Locate and identify every blood parasite.
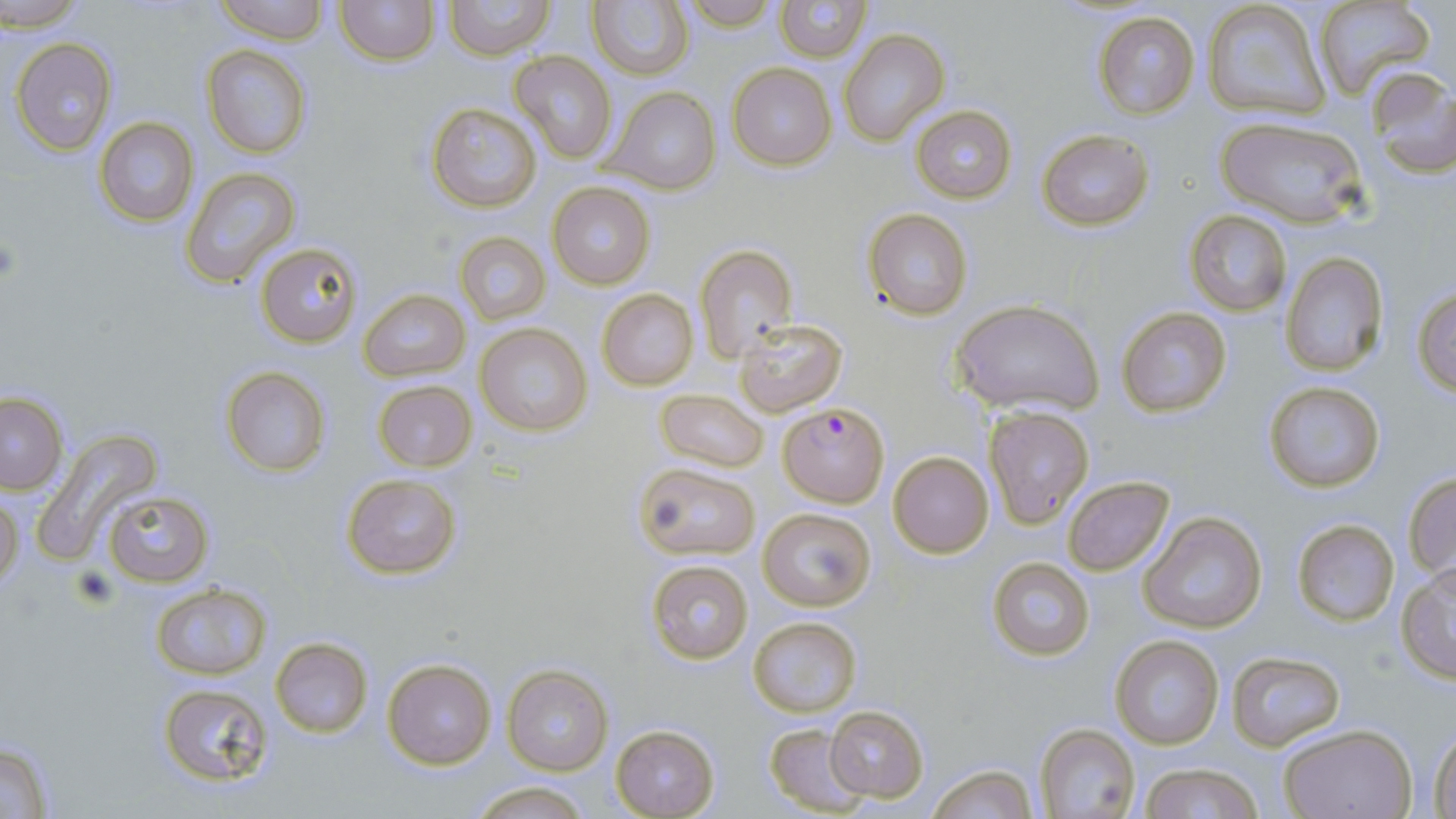
Approximate bounding boxes as (x1,y1)-(x2,y2) corner pairs in pixels.
Plasmodium falciparum-infected red blood cells: (778,403)-(890,505).
No Plasmodium ovale, Plasmodium malariae, Plasmodium vivax, Babesia divergens, or Trypanosoma brucei observed.

Uninfected red blood cell locations: (4,0)-(88,31), (212,0)-(329,44), (334,0)-(439,66), (681,0)-(780,31), (774,0)-(869,61), (1315,0)-(1436,102), (443,1)-(554,60), (1200,2)-(1331,120), (588,3)-(693,79), (1093,11)-(1200,118), (840,29)-(949,145), (10,37)-(118,154), (202,44)-(312,159), (509,50)-(617,165), (728,64)-(836,169), (1366,68)-(1456,180), (604,86)-(719,194), (425,102)-(542,213), (911,105)-(1017,202), (1215,114)-(1367,228), (94,116)-(200,226), (1038,129)-(1153,232), (180,167)-(302,286), (547,180)-(657,291), (862,209)-(974,320), (1185,210)-(1292,315), (455,231)-(550,325), (257,242)-(362,347), (695,244)-(798,362), (1279,252)-(1389,376), (1412,287)-(1456,397), (597,288)-(699,392), (358,290)-(469,380), (951,298)-(1104,418), (1116,306)-(1233,418), (734,318)-(848,415), (477,323)-(592,438), (219,365)-(332,478), (372,379)-(476,473), (1262,381)-(1386,494), (656,389)-(768,473), (0,393)-(66,494), (983,407)-(1094,529), (36,426)-(163,558), (889,452)-(993,558), (634,463)-(759,560), (343,472)-(462,580), (1403,474)-(1456,579), (1062,476)-(1175,576), (101,490)-(213,588), (0,493)-(22,589), (759,507)-(877,612), (1138,511)-(1267,634), (1292,518)-(1399,625), (987,556)-(1094,661), (645,560)-(755,665), (1397,565)-(1456,683), (149,582)-(273,678), (747,616)-(862,717), (1110,635)-(1223,750), (269,637)-(374,738), (1227,652)-(1345,749), (383,658)-(497,769), (501,663)-(613,776), (155,682)-(279,790), (826,706)-(929,801), (1032,722)-(1142,819), (609,723)-(720,818), (764,724)-(869,815), (1279,724)-(1415,818), (1429,728)-(1456,818), (0,738)-(55,817), (927,763)-(1037,818), (1139,764)-(1264,819), (466,782)-(594,817). Slide-level diagnosis: Plasmodium falciparum. 1000x magnification. Thin blood film. Image is 1456×819 pixels. Single field of view. May-Grünwald-Giemsa-stained preparation. Optical microscopy.